Outline each uninfected red blood cell.
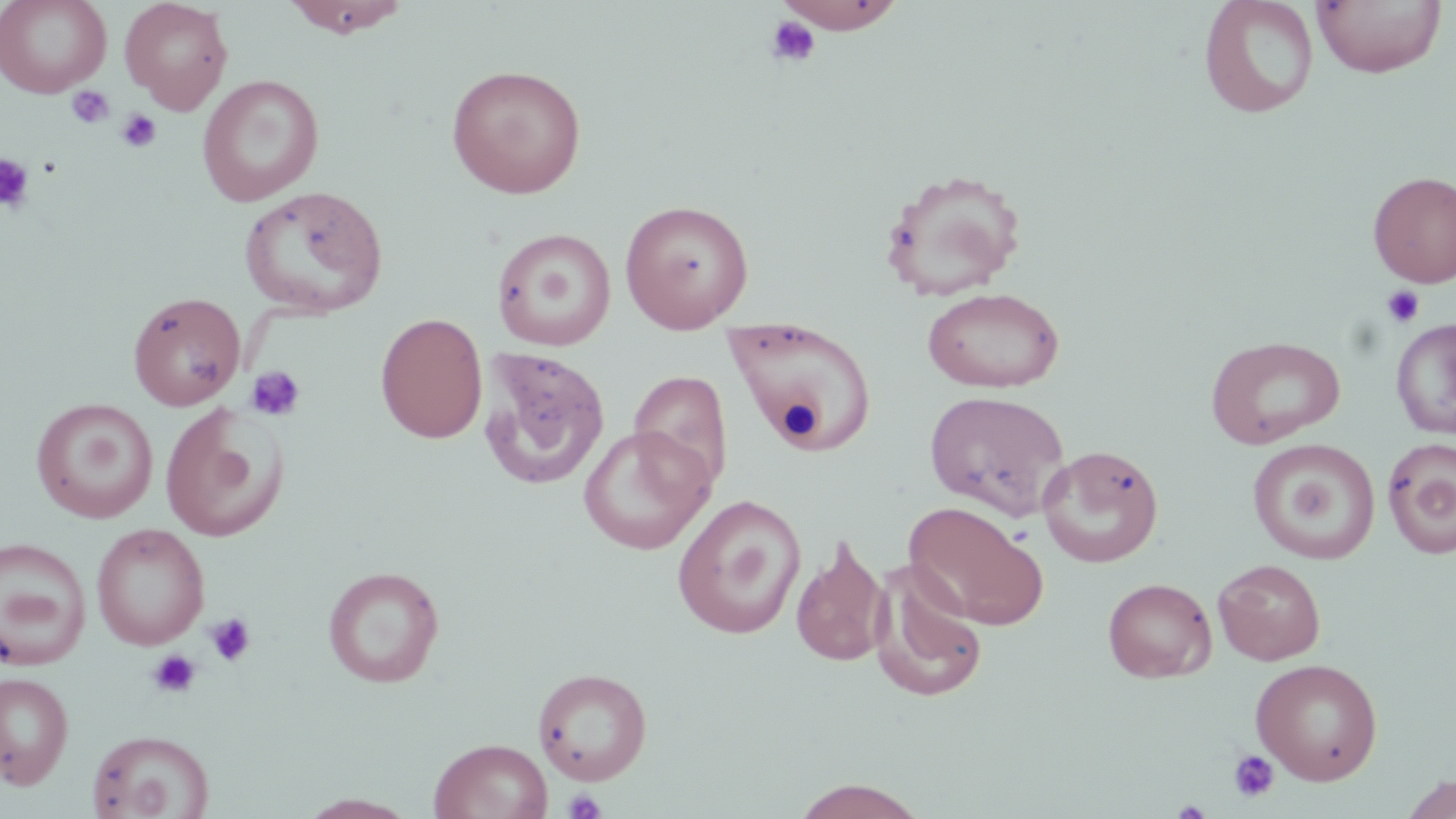

Approximate bounding boxes as named x1/y1/x2/y2 corners in pixels.
Uninfected red blood cells: (x1=0, y1=0, x2=111, y2=97), (x1=120, y1=0, x2=233, y2=114), (x1=281, y1=0, x2=412, y2=38), (x1=774, y1=0, x2=907, y2=33), (x1=1197, y1=0, x2=1320, y2=120), (x1=1312, y1=0, x2=1447, y2=78), (x1=0, y1=1, x2=233, y2=101), (x1=445, y1=64, x2=587, y2=199), (x1=197, y1=74, x2=324, y2=206), (x1=880, y1=168, x2=1028, y2=301), (x1=1368, y1=171, x2=1456, y2=287), (x1=239, y1=185, x2=388, y2=319), (x1=619, y1=199, x2=755, y2=333), (x1=490, y1=222, x2=755, y2=346), (x1=492, y1=226, x2=617, y2=351), (x1=922, y1=287, x2=1064, y2=393), (x1=127, y1=291, x2=246, y2=411), (x1=375, y1=312, x2=488, y2=444), (x1=724, y1=316, x2=878, y2=451), (x1=1391, y1=317, x2=1456, y2=439), (x1=1206, y1=335, x2=1345, y2=449), (x1=479, y1=347, x2=610, y2=492), (x1=629, y1=369, x2=734, y2=494), (x1=923, y1=390, x2=1070, y2=521), (x1=30, y1=398, x2=158, y2=523), (x1=159, y1=402, x2=290, y2=543), (x1=578, y1=425, x2=714, y2=555), (x1=1382, y1=437, x2=1456, y2=559), (x1=1248, y1=438, x2=1381, y2=565), (x1=1036, y1=444, x2=1164, y2=568), (x1=672, y1=494, x2=807, y2=640), (x1=903, y1=501, x2=1050, y2=631), (x1=91, y1=523, x2=210, y2=651), (x1=790, y1=533, x2=891, y2=669), (x1=0, y1=536, x2=92, y2=670), (x1=1213, y1=558, x2=1326, y2=665), (x1=869, y1=562, x2=988, y2=703), (x1=323, y1=565, x2=445, y2=688), (x1=1102, y1=578, x2=1216, y2=683), (x1=1250, y1=658, x2=1384, y2=785), (x1=533, y1=667, x2=653, y2=785), (x1=0, y1=671, x2=75, y2=790), (x1=86, y1=729, x2=215, y2=819), (x1=429, y1=738, x2=553, y2=819), (x1=1398, y1=772, x2=1456, y2=818), (x1=789, y1=778, x2=930, y2=819), (x1=297, y1=793, x2=421, y2=818).

slide-level diagnosis = negative for blood parasites
platelet locations = approximate bounding boxes as named x1/y1/x2/y2 corners in pixels: (x1=765, y1=15, x2=821, y2=68), (x1=66, y1=86, x2=114, y2=130), (x1=116, y1=109, x2=161, y2=153), (x1=0, y1=153, x2=36, y2=213), (x1=1381, y1=284, x2=1425, y2=328), (x1=245, y1=365, x2=306, y2=422), (x1=205, y1=612, x2=257, y2=667), (x1=147, y1=649, x2=201, y2=698), (x1=1228, y1=749, x2=1279, y2=802), (x1=563, y1=788, x2=606, y2=819)
field of view = single
image size = 1456×819 pixels
magnification = 1000x
stain = May-Grünwald-Giemsa
modality = light microscopy
preparation = thin blood film